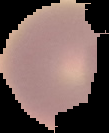

Result: no malaria parasites seen. From a thin blood film. Image is 109×133 pixels. Segmented cell region on a black background.